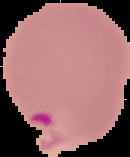

{
  "image_size": "130×157 pixels",
  "malaria_status": "parasitized",
  "preparation": "thin blood smear",
  "image_type": "segmented cell region with the area outside set to black"
}